Name the blood parasite species.
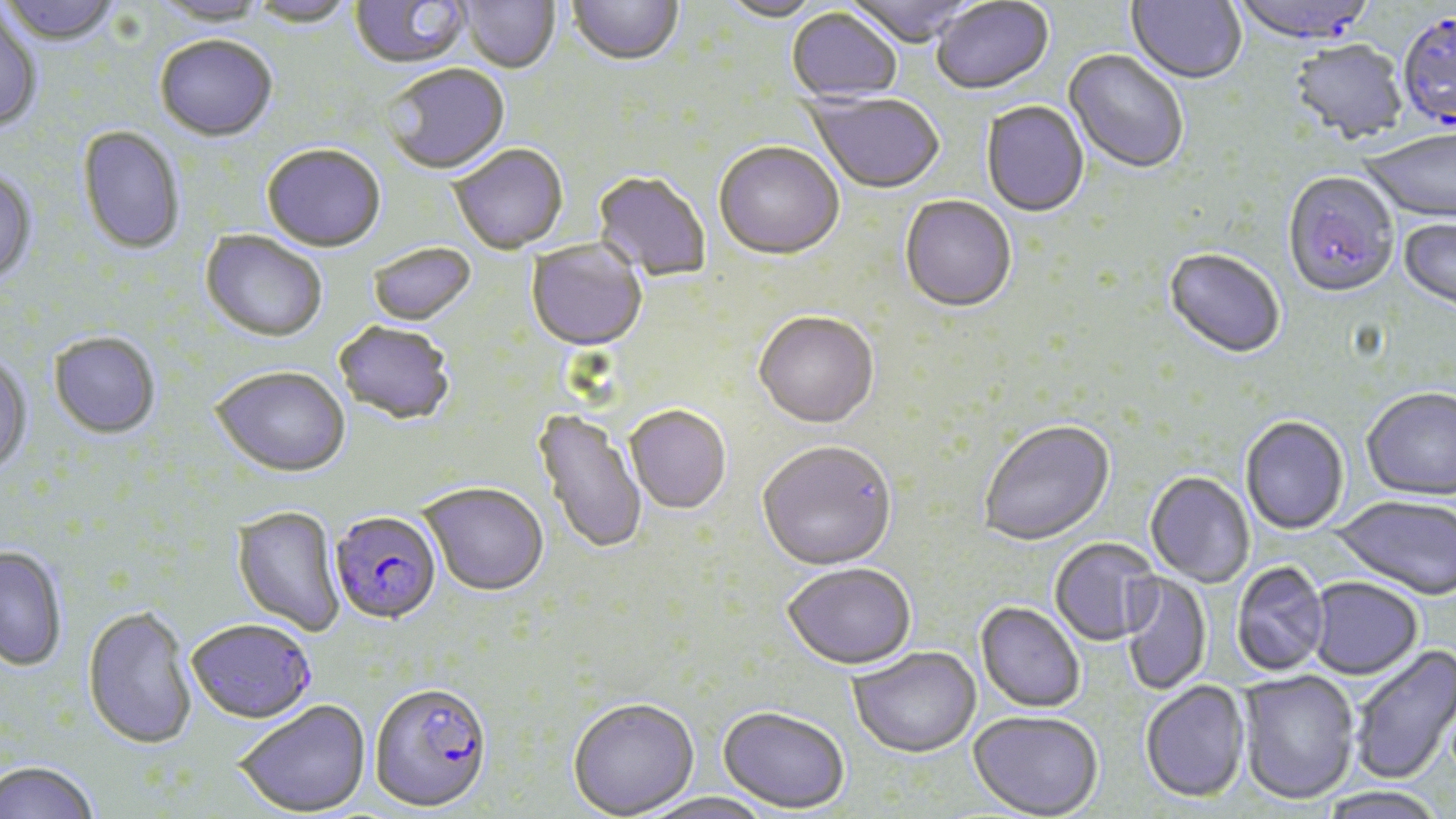

Plasmodium falciparum.

Summary:
  - Coordinate format: approximate bounding boxes as (x1, y1, x2, y2) in pixels
  - Plasmodium falciparum-infected red blood cell locations: (1232, 0, 1378, 48), (1396, 13, 1456, 134), (329, 512, 443, 627), (186, 621, 317, 726), (369, 685, 492, 815)
  - Uninfected red blood cell locations: (1, 0, 121, 48), (154, 0, 268, 28), (248, 0, 356, 29), (349, 0, 471, 72), (460, 0, 560, 75), (567, 0, 683, 69), (718, 0, 827, 24), (844, 0, 978, 50), (1126, 0, 1246, 87), (930, 1, 1054, 97), (786, 8, 901, 104), (0, 10, 43, 133), (155, 38, 277, 145), (1289, 41, 1408, 146), (1062, 50, 1188, 176), (383, 65, 511, 177), (805, 91, 944, 196), (981, 102, 1089, 219), (77, 127, 185, 256), (1360, 129, 1456, 226), (714, 144, 844, 263), (261, 146, 386, 254), (450, 146, 568, 256), (0, 171, 37, 286), (592, 173, 710, 281), (1283, 173, 1399, 300), (899, 197, 1016, 314), (1398, 219, 1456, 315), (200, 232, 327, 345), (526, 240, 648, 354), (367, 244, 476, 328), (1164, 250, 1285, 361), (753, 314, 880, 431), (334, 323, 455, 427), (49, 333, 160, 440), (0, 357, 33, 479), (211, 368, 350, 480), (1362, 388, 1456, 503), (625, 407, 731, 516), (533, 408, 648, 556), (1241, 418, 1349, 536), (978, 421, 1116, 547), (757, 443, 897, 573), (1145, 472, 1255, 588), (418, 484, 548, 598), (1332, 496, 1456, 601), (232, 506, 345, 637), (1050, 539, 1160, 647), (0, 546, 67, 672), (1231, 562, 1330, 676), (783, 565, 916, 672), (1122, 573, 1212, 696), (1308, 577, 1423, 680), (975, 602, 1084, 713), (81, 606, 197, 752), (1348, 643, 1456, 785), (848, 648, 982, 760), (1238, 669, 1360, 804), (1140, 680, 1251, 804), (567, 699, 700, 819), (235, 702, 371, 817), (718, 709, 850, 815), (968, 711, 1103, 819), (0, 761, 100, 819), (1318, 786, 1445, 819), (642, 793, 776, 819)
  - Magnification: 1000x
  - Modality: light microscopy
  - Stain: May-Grünwald-Giemsa
  - Field of view: one of a larger specimen
  - Preparation: thin blood film
  - Image size: 1456×819 pixels